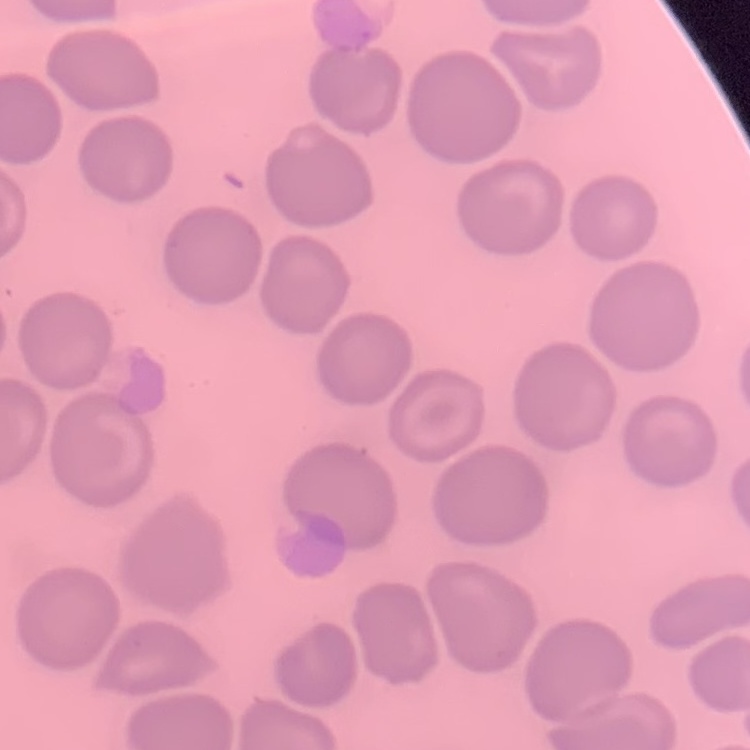

The red blood cells exhibit no rouleaux formation. Field's or Giemsa stain. One tile cut from a larger photomicrograph. Thin blood film.